Report the malaria status of this cell.
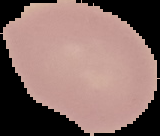

Uninfected.

Summary:
  - Image type: cell region segmented out of the field of view; surrounding area masked to black
  - Image size: 160×136 pixels
  - Preparation: thin blood smear